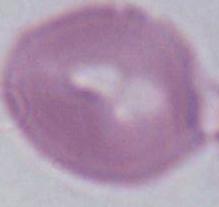
1000x magnification. An erythrocyte is shown. Photomicrograph.